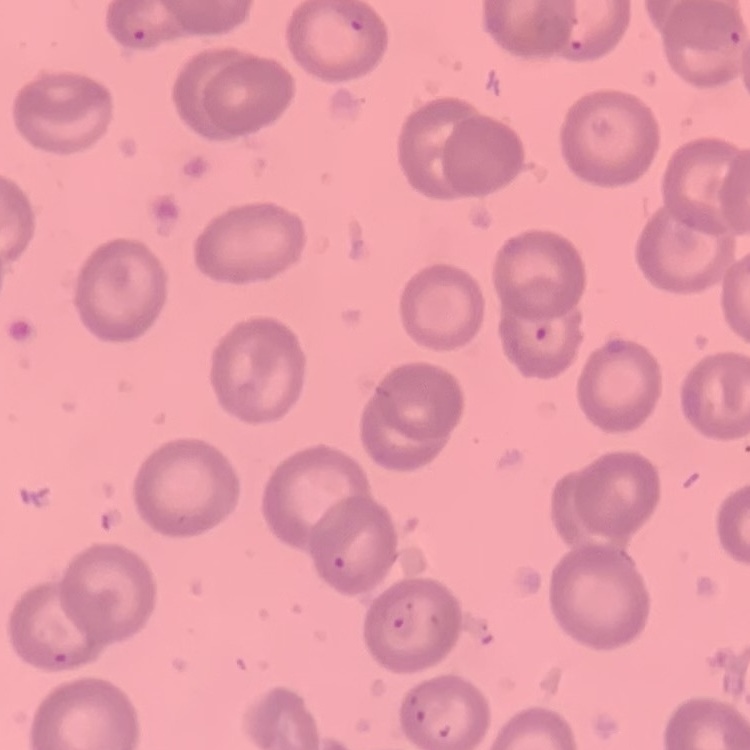
Summary:
  - Red blood cell morphology: no rouleaux formation
  - Image type: square crop of a larger photomicrograph
  - Stain: Field's or Giemsa
  - Preparation: thin blood film